Name the blood parasite species.
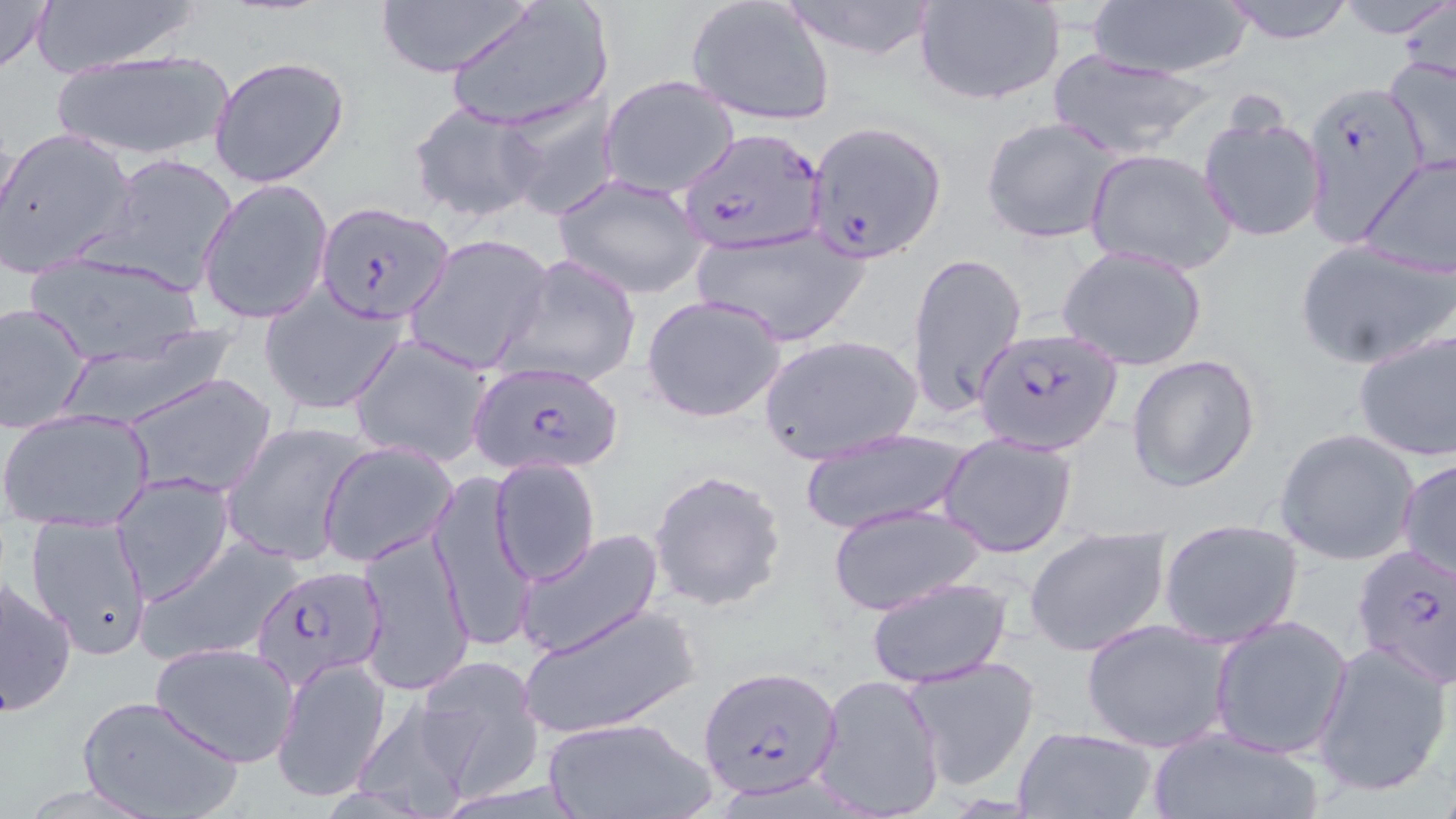
Plasmodium falciparum.

Approximate bounding boxes as [x1, y1, x2, y2] in pixels. Plasmodium falciparum-infected red blood cell locations: [1301, 79, 1428, 240], [802, 121, 945, 261], [679, 126, 828, 255], [315, 203, 454, 325], [906, 246, 1028, 423], [972, 328, 1123, 453], [467, 359, 628, 476], [1351, 545, 1456, 690], [251, 562, 386, 689], [699, 666, 843, 799]. Uninfected red blood cell locations: [0, 0, 54, 77], [23, 0, 206, 76], [776, 0, 942, 61], [917, 0, 1066, 106], [1082, 0, 1257, 79], [1217, 0, 1358, 44], [1333, 0, 1456, 40], [444, 1, 613, 133], [685, 1, 836, 127], [375, 2, 532, 77], [1394, 2, 1456, 92], [50, 45, 235, 164], [1382, 50, 1456, 175], [1042, 53, 1221, 161], [209, 55, 352, 189], [599, 76, 740, 199], [500, 95, 619, 221], [407, 102, 545, 225], [1196, 109, 1327, 244], [981, 115, 1124, 246], [0, 127, 136, 276], [1085, 149, 1236, 275], [1360, 151, 1456, 277], [91, 153, 239, 298], [554, 173, 711, 299], [197, 178, 332, 326], [692, 228, 872, 347], [405, 233, 554, 376], [1295, 237, 1456, 370], [1057, 243, 1210, 371], [23, 251, 210, 368], [497, 253, 642, 391], [259, 288, 407, 418], [640, 294, 789, 424], [1, 301, 93, 432], [1352, 327, 1456, 462], [758, 332, 922, 464], [348, 333, 497, 468], [1126, 353, 1262, 491], [123, 371, 278, 499], [0, 407, 155, 529], [220, 418, 371, 568], [796, 428, 971, 536], [1274, 428, 1421, 566], [939, 433, 1077, 557], [319, 441, 457, 566], [1398, 457, 1456, 581], [489, 458, 601, 585], [648, 468, 787, 613], [430, 469, 536, 652], [110, 474, 234, 605], [826, 502, 985, 616], [22, 515, 155, 658], [1156, 519, 1304, 649], [1023, 524, 1173, 658], [356, 527, 473, 695], [514, 527, 667, 659], [137, 534, 305, 667], [1, 574, 77, 716], [864, 576, 1013, 689], [520, 600, 701, 738], [1208, 614, 1353, 760], [1081, 618, 1232, 753], [1312, 639, 1454, 799], [150, 640, 301, 769], [273, 655, 390, 802], [416, 655, 544, 798], [902, 655, 1042, 790], [812, 673, 945, 819], [78, 695, 245, 819], [348, 698, 478, 816], [540, 715, 717, 819], [1145, 724, 1324, 819], [1010, 725, 1160, 819]. Image is 1456×819 pixels. May-Grünwald-Giemsa-stained preparation. Thin blood film. Optical microscopy. 1000x magnification. One field of a larger specimen.